Comment on the morphology of the red blood cells.
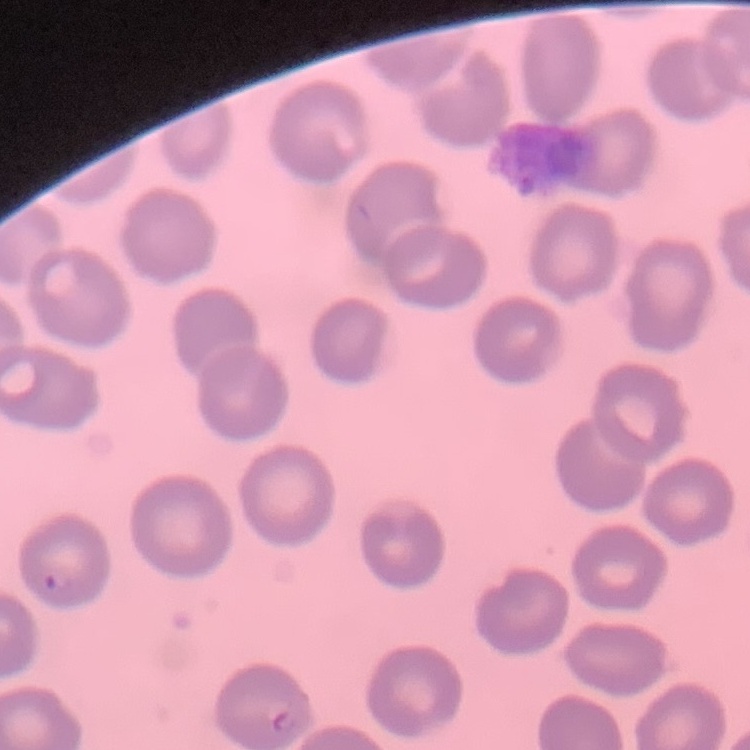
No rouleaux formation.

Summary:
  - Image type: one tile cut from a larger photomicrograph
  - Stain: Field's or Giemsa
  - Preparation: thin blood film